Give the extent of all Plasmodium ovale-infected red blood cells.
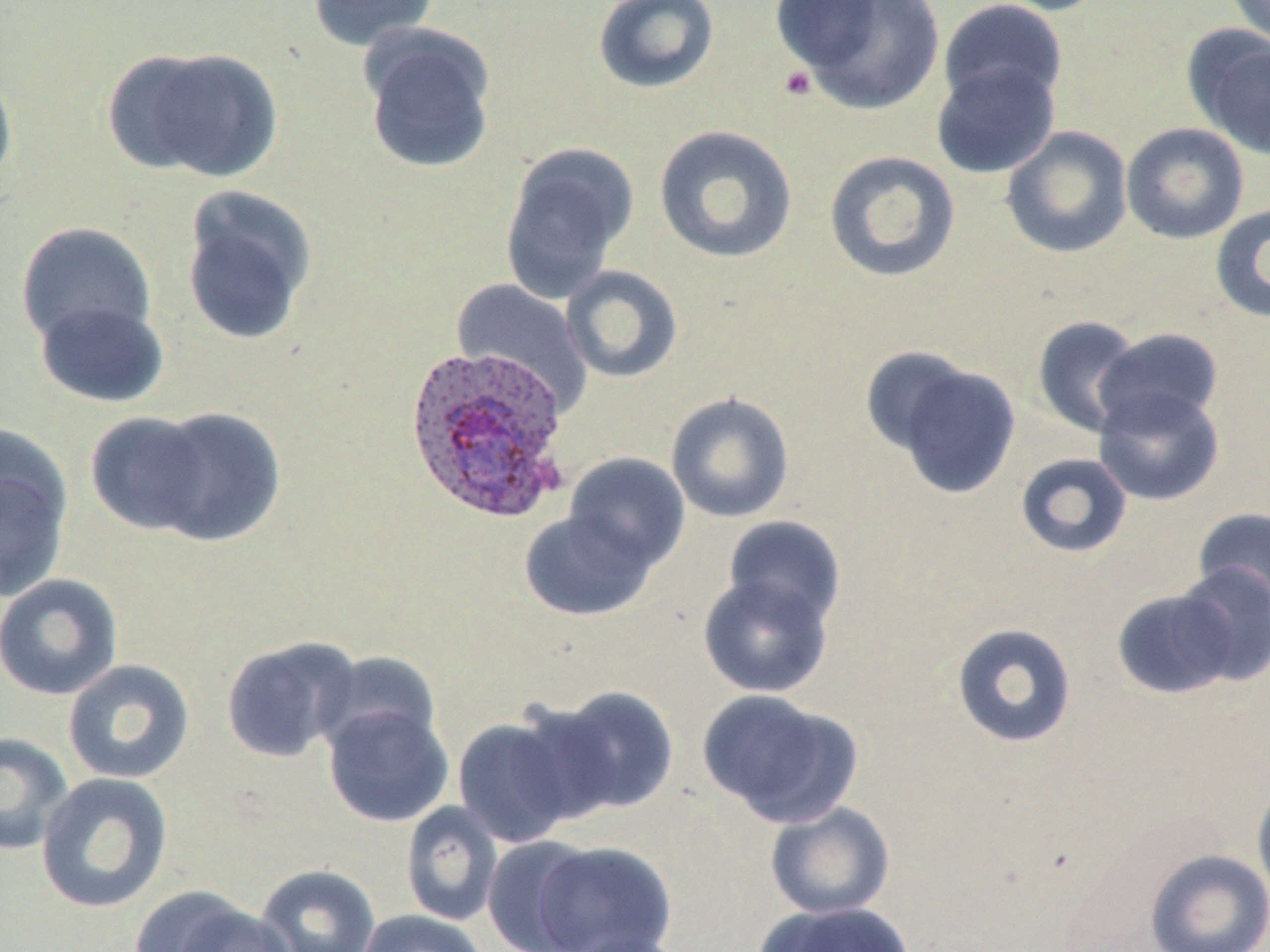

Approximate bounding boxes as (x1,y1)-(x2,y2) corner pairs in pixels.
Plasmodium ovale-infected red blood cells: (404,343)-(572,523).

Summary:
  - Uninfected red blood cell locations: (308,0)-(440,51), (592,0)-(720,94), (779,0)-(945,115), (937,0)-(1069,114), (981,0)-(1110,16), (1225,1)-(1270,48), (359,25)-(497,174), (1184,27)-(1270,162), (108,46)-(283,184), (931,60)-(1061,180), (0,66)-(18,195), (1121,122)-(1249,245), (654,124)-(798,264), (1000,126)-(1133,259), (499,142)-(639,302), (823,150)-(961,283), (179,186)-(318,346), (1210,203)-(1270,324), (15,221)-(158,348), (561,264)-(683,383), (452,279)-(593,412), (34,297)-(170,408), (1032,315)-(1144,438), (1094,327)-(1224,433), (868,351)-(1023,500), (1093,387)-(1225,506), (666,391)-(795,523), (145,406)-(286,547), (84,411)-(216,537), (0,440)-(73,604), (563,452)-(690,572), (1015,452)-(1133,558), (1192,507)-(1270,613), (519,509)-(657,621), (723,516)-(846,629), (1174,562)-(1270,686), (698,571)-(834,697), (0,574)-(123,700), (1110,586)-(1240,700), (951,622)-(1078,749), (220,636)-(361,763), (315,650)-(443,755), (62,659)-(195,784), (544,685)-(680,819), (697,689)-(862,828), (321,702)-(454,827), (451,713)-(585,848), (0,732)-(74,856), (35,772)-(174,914), (1252,778)-(1270,907), (400,801)-(504,927), (764,802)-(897,919), (480,835)-(600,952), (525,839)-(678,951), (1144,848)-(1270,952), (255,864)-(380,952), (136,890)-(298,952), (754,900)-(911,951), (355,909)-(490,952), (563,930)-(693,952)
  - Platelet locations: (777,65)-(816,100)
  - Slide-level diagnosis: Plasmodium ovale
  - Image size: 1270×952 pixels
  - Field of view: one of a larger specimen
  - Stain: May-Grünwald-Giemsa
  - Modality: light microscopy
  - Preparation: thin blood smear
  - Magnification: 1000x